Report the malaria status of this cell.
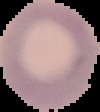

Uninfected.

Summary:
  - Image size: 100×112 pixels
  - Image type: cell region segmented out of the field of view; surrounding area masked to black
  - Preparation: thin blood smear